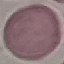

Summary:
  - Result: no malaria parasites seen
  - Stain: Giemsa
  - Image type: automatically extracted cell patch, resized to 64 × 64 pixels
  - Capture: smartphone camera at the microscope eyepiece
  - Preparation: thin smear